State which parasite is depicted.
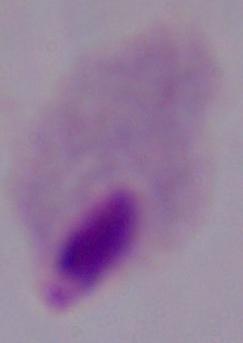

A trichomonad.

Summary:
  - Magnification: 1000x
  - Modality: micrograph